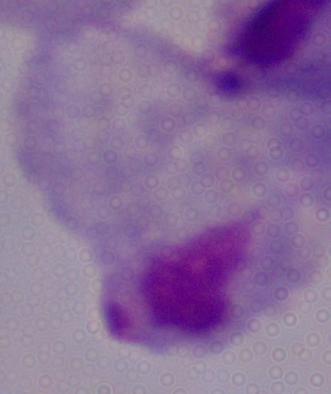

Summary:
  - Modality: photomicrograph
  - Identification: trichomonad
  - Magnification: 1000x